Classify this cell by malaria status.
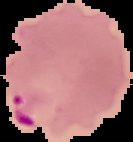

Parasitized.

image type = segmented cell region with the area outside set to black
preparation = thin blood smear
image size = 133×142 pixels